Locate every uninfected red blood cell.
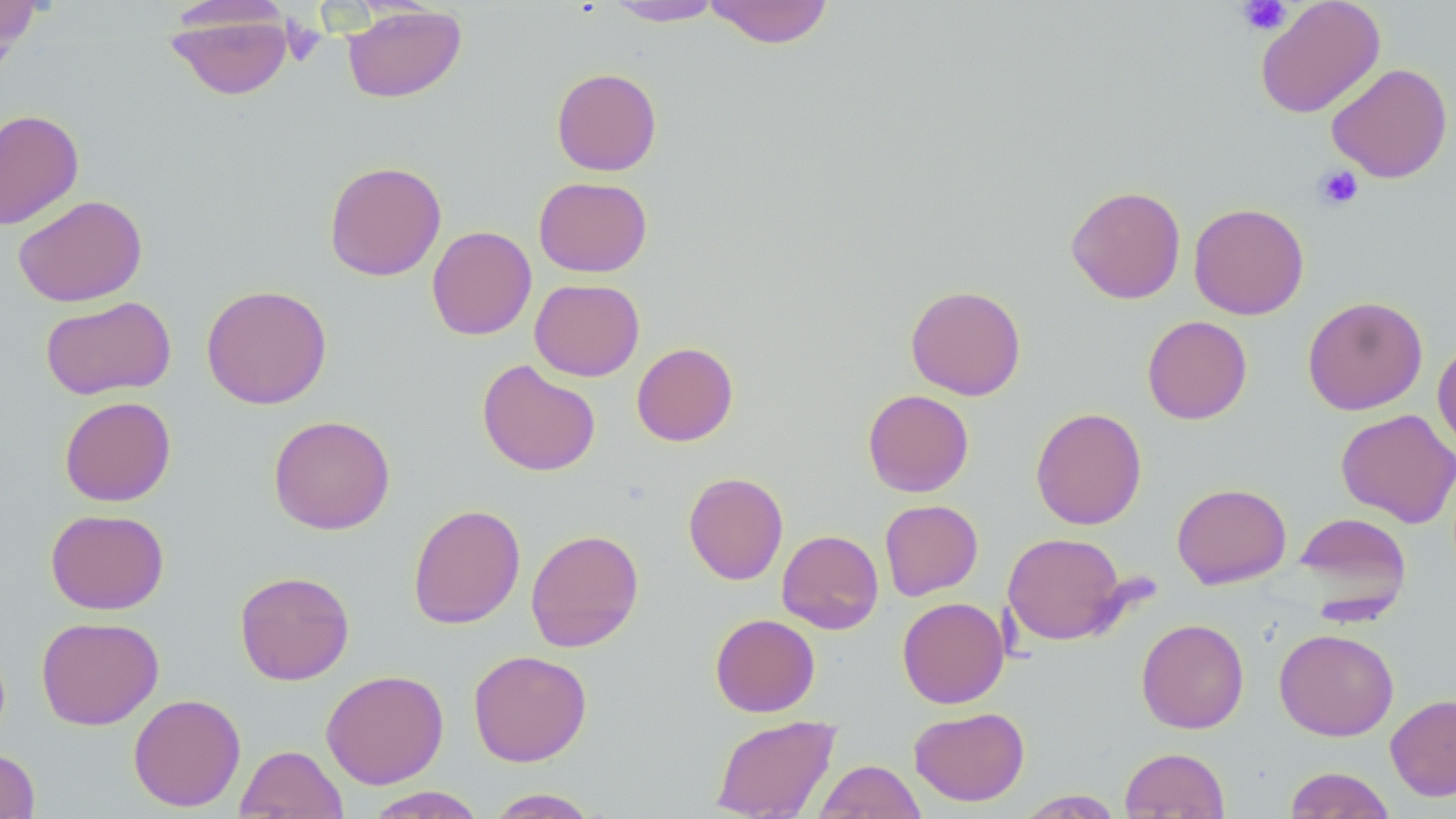

Approximate bounding boxes as (x1,y1)-(x2,y2) corner pairs in pixels.
Uninfected red blood cells: (0,0)-(41,67), (605,0)-(724,26), (703,0)-(835,49), (1255,0)-(1385,118), (165,4)-(295,101), (342,5)-(467,103), (1327,63)-(1453,183), (551,67)-(662,176), (0,108)-(84,230), (324,160)-(446,281), (534,176)-(652,277), (1065,185)-(1186,304), (13,194)-(147,307), (1189,203)-(1309,320), (426,225)-(537,340), (529,278)-(645,381), (200,284)-(332,410), (905,284)-(1026,400), (40,296)-(176,400), (1302,296)-(1429,415), (1142,315)-(1252,424), (1432,336)-(1456,455), (631,342)-(738,446), (477,359)-(601,477), (862,389)-(974,497), (59,396)-(176,506), (1030,407)-(1146,530), (1335,409)-(1456,528), (268,414)-(396,535), (683,472)-(788,585), (1172,482)-(1292,589), (879,499)-(983,600), (408,504)-(525,629), (45,509)-(169,614), (1294,511)-(1413,618), (526,529)-(644,652), (776,529)-(884,634), (1002,532)-(1130,645), (234,570)-(355,685), (897,597)-(1009,709), (710,613)-(820,717), (36,616)-(164,730), (1136,618)-(1249,734), (1274,628)-(1399,740), (468,649)-(592,767), (321,669)-(449,789), (128,693)-(246,812), (1386,693)-(1456,801), (909,706)-(1029,806), (711,715)-(840,818), (235,744)-(348,819), (1119,746)-(1230,818), (0,749)-(40,818), (814,759)-(925,819), (1284,766)-(1397,818), (363,786)-(487,818), (485,788)-(601,818), (1015,789)-(1124,818).

Platelet locations: (1237,0)-(1292,36), (280,19)-(325,66), (1313,164)-(1364,211). Slide-level diagnosis: no evidence of blood parasites. Image is 1456×819 pixels. Thin blood film. Light microscopy. Single field of view. May-Grünwald-Giemsa stain. Captured at 1000x magnification.